Report the malaria status.
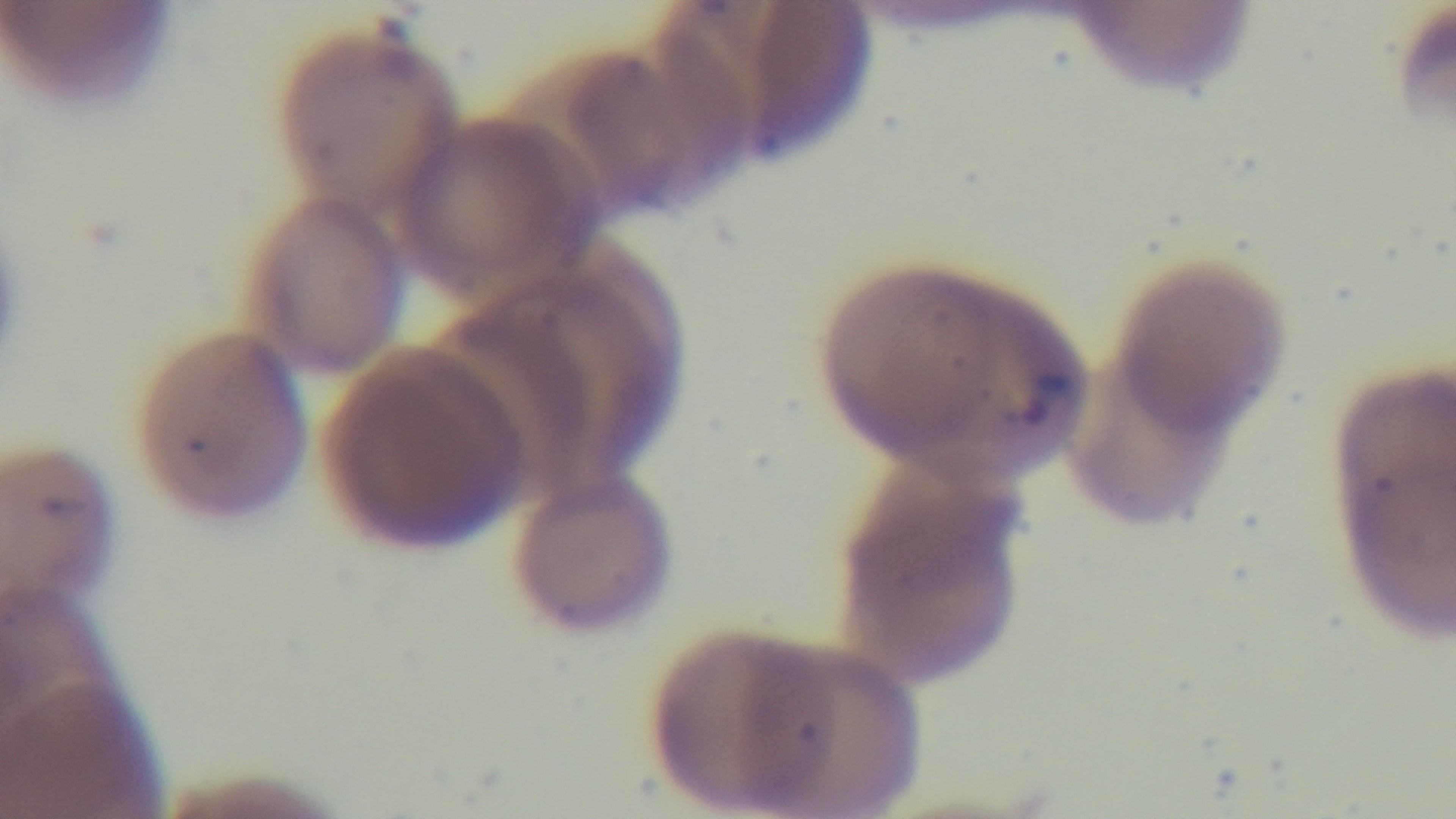
Positive.

Light microscopy. Captured with a mounted 4K digital camera. Giemsa stain. Preparation: thin blood film. One field from the slide. Oil-immersion objective, 100x.